Locate every blood parasite and identify its species.
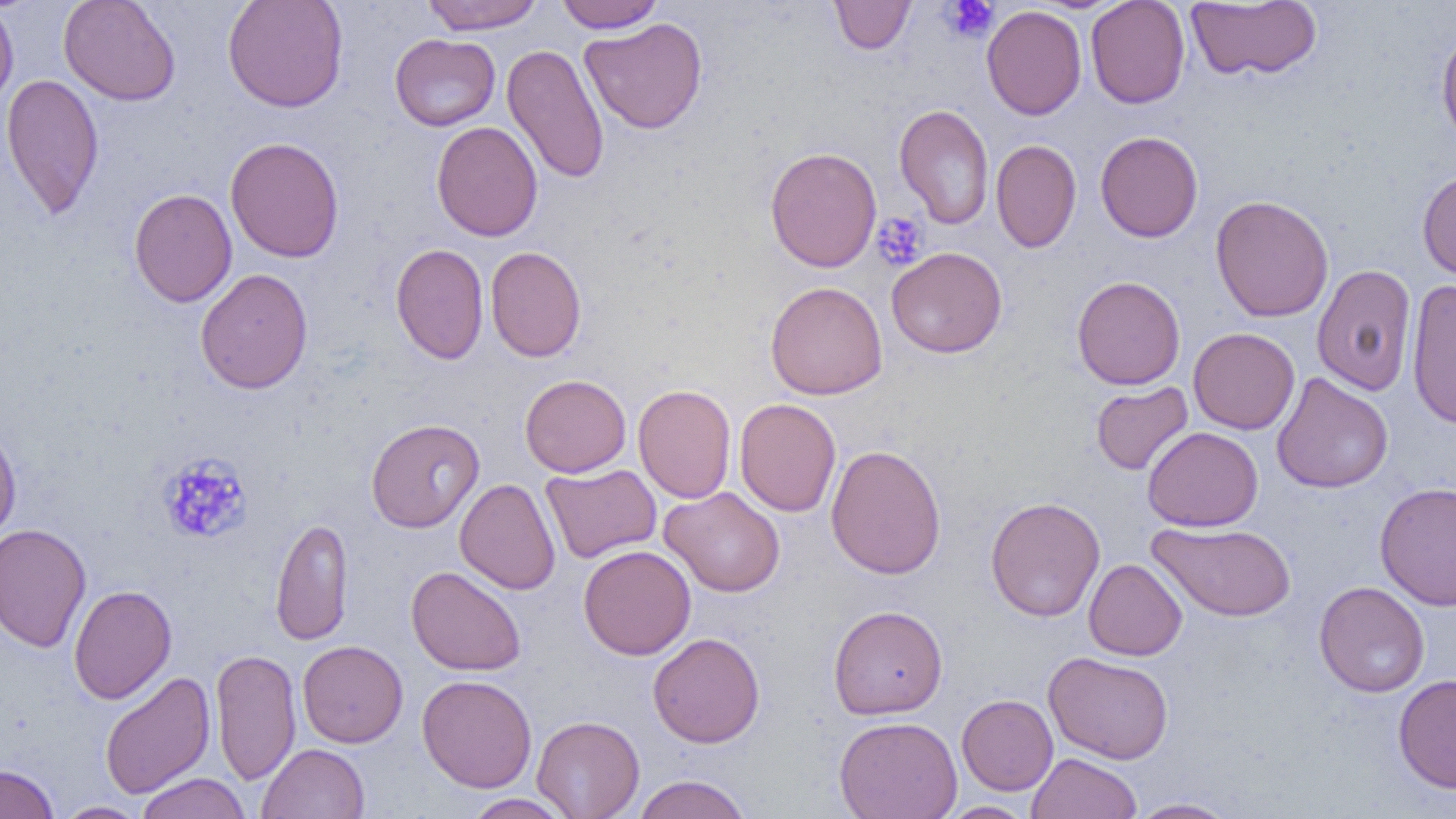
No blood parasites seen.

Approximate bounding boxes as (x1,y1)-(x2,y2) corner pairs in pixels. Uninfected red blood cell locations: (58,0)-(181,106), (222,0)-(349,112), (420,0)-(544,34), (553,0)-(666,33), (829,0)-(916,54), (1085,0)-(1190,108), (0,1)-(19,112), (1185,1)-(1322,82), (982,5)-(1087,120), (579,17)-(708,134), (1436,24)-(1456,149), (390,34)-(500,131), (502,43)-(610,185), (1,73)-(104,220), (894,104)-(994,229), (431,121)-(543,242), (1095,130)-(1203,242), (225,137)-(344,263), (991,139)-(1082,253), (765,146)-(882,272), (1417,170)-(1456,282), (128,188)-(238,307), (1210,195)-(1334,322), (390,243)-(489,364), (485,246)-(586,362), (886,246)-(1007,358), (1312,264)-(1416,396), (195,268)-(313,394), (1072,275)-(1185,390), (1406,279)-(1456,430), (765,281)-(888,400), (1188,328)-(1300,434), (1271,372)-(1393,494), (520,374)-(631,477), (1090,381)-(1193,476), (632,384)-(737,504), (734,398)-(841,517), (365,418)-(484,532), (0,423)-(22,545), (1142,426)-(1263,532), (825,444)-(946,580), (540,463)-(661,563), (455,478)-(561,595), (1374,481)-(1456,611), (659,486)-(786,598), (985,496)-(1106,621), (270,516)-(353,645), (1149,521)-(1296,621), (0,523)-(92,653), (578,544)-(696,660), (1083,558)-(1187,661), (406,566)-(526,676), (1314,581)-(1430,697), (68,584)-(177,705), (828,605)-(948,719), (647,632)-(765,748), (297,640)-(408,747), (210,648)-(302,786), (1044,651)-(1174,764), (99,670)-(215,798), (1393,673)-(1456,793), (417,674)-(537,793), (956,694)-(1058,795), (532,715)-(645,819), (834,715)-(962,819), (257,743)-(369,819), (1027,752)-(1142,819), (0,764)-(59,819), (135,773)-(252,819), (632,774)-(752,819), (462,794)-(574,818), (1126,797)-(1240,818), (54,801)-(150,818), (940,801)-(1036,818). Platelet locations: (941,0)-(1000,42), (872,211)-(929,270), (156,452)-(254,544). Slide-level diagnosis: negative for blood parasites. 1000x magnification. One field of a larger specimen. Thin blood smear. Image is 1456×819 pixels. Optical microscopy.